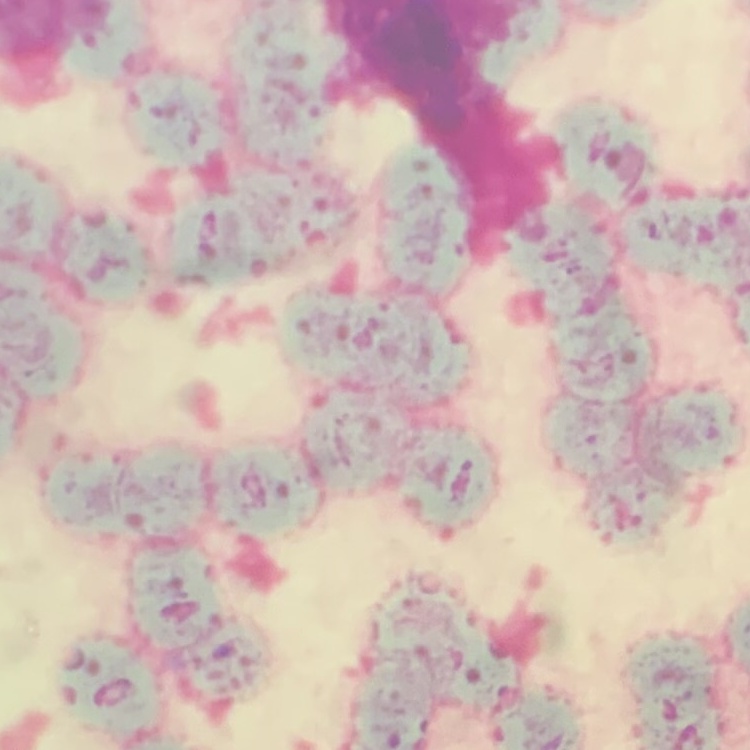
{
  "red_blood_cell_morphology": "rouleaux formation",
  "image_type": "one tile cut from a larger photomicrograph",
  "preparation": "thin blood smear",
  "stain": "Field's or Giemsa"
}